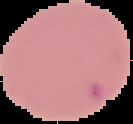
image_size: 133×124 pixels
preparation: thin blood smear
malaria_status: uninfected
image_type: cell region segmented out of the field of view; surrounding area masked to black